Classify this cell by malaria status.
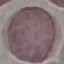

It is uninfected.

image type = cell patch, automatically extracted from a larger field of view and resized to 64 × 64 pixels
capture = smartphone through the microscope eyepiece
stain = Giemsa
preparation = thin smear